Report the malaria status of this cell.
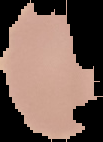
It is uninfected.

Image is 103×142 pixels. From a thin blood film. Segmented cell region on a black background.